Outline each blood parasite and name the species.
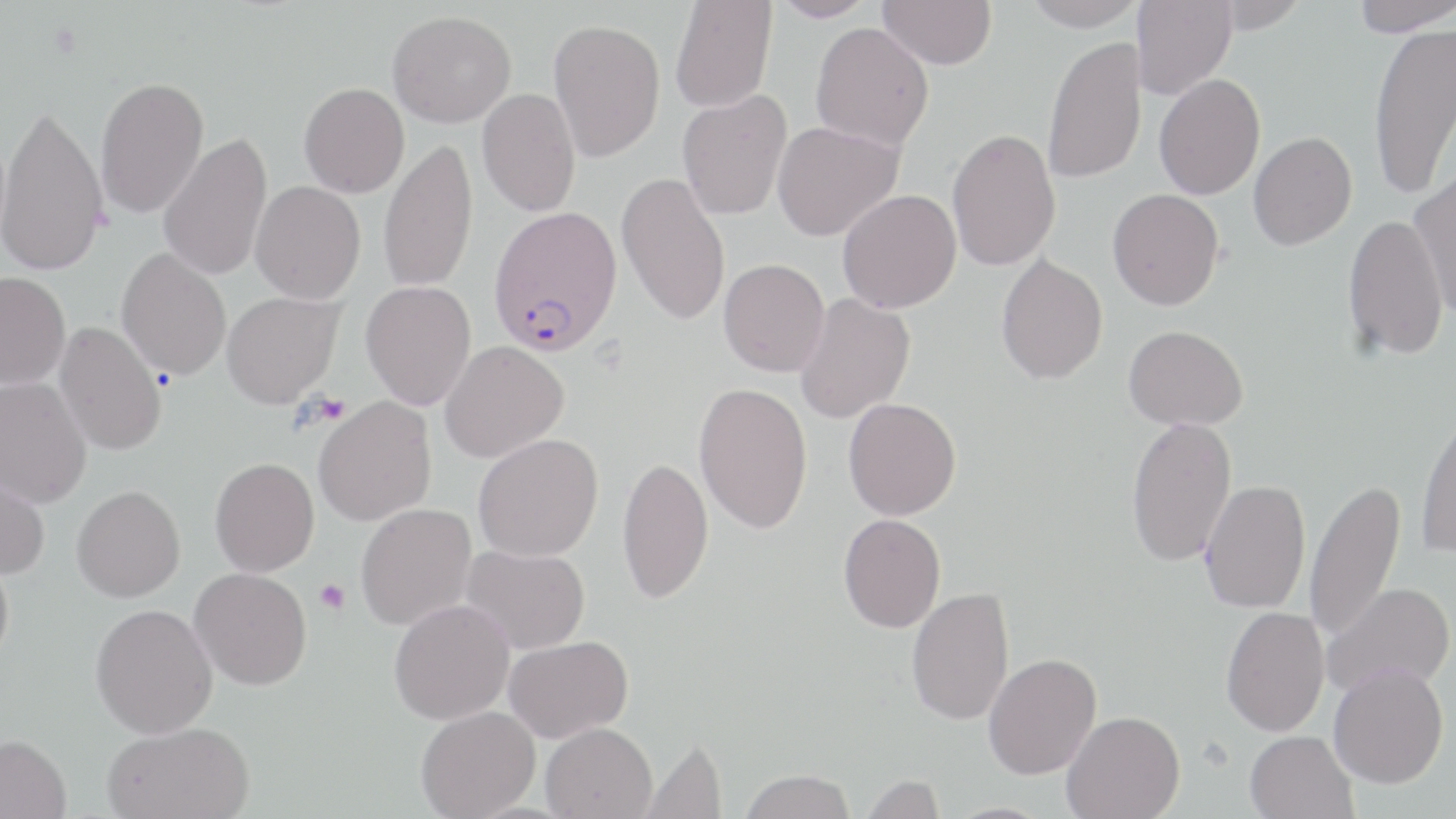

Approximate bounding boxes as [x1, y1, x2, y2] in pixels.
Plasmodium falciparum-infected red blood cells: [489, 205, 623, 356].
No Plasmodium ovale, Plasmodium malariae, Plasmodium vivax, Babesia divergens, or Trypanosoma brucei observed.

Uninfected red blood cell locations: [669, 0, 777, 113], [770, 0, 878, 22], [878, 0, 997, 70], [1021, 0, 1144, 31], [1133, 0, 1236, 100], [1207, 0, 1311, 33], [1349, 0, 1456, 37], [387, 10, 516, 128], [548, 18, 665, 161], [810, 22, 934, 152], [1368, 22, 1456, 202], [1042, 35, 1146, 184], [1153, 74, 1265, 200], [94, 76, 209, 219], [299, 82, 409, 198], [477, 89, 581, 217], [677, 90, 792, 219], [0, 102, 109, 277], [772, 121, 904, 242], [947, 128, 1061, 271], [158, 132, 273, 282], [1248, 132, 1357, 250], [378, 138, 478, 293], [1409, 169, 1456, 318], [616, 171, 731, 326], [250, 181, 366, 304], [837, 189, 962, 313], [1107, 189, 1224, 310], [1342, 214, 1449, 361], [116, 246, 232, 382], [996, 253, 1108, 385], [719, 258, 830, 377], [0, 271, 71, 389], [360, 280, 476, 409], [222, 292, 343, 408], [794, 292, 916, 424], [53, 321, 168, 456], [1124, 325, 1248, 430], [440, 341, 568, 462], [0, 377, 93, 508], [694, 382, 813, 534], [313, 396, 436, 526], [843, 398, 961, 520], [1415, 407, 1456, 559], [1125, 416, 1237, 566], [473, 433, 604, 561], [617, 456, 714, 604], [210, 457, 319, 576], [0, 466, 50, 581], [1304, 478, 1405, 645], [1199, 479, 1311, 613], [72, 485, 185, 602], [355, 503, 477, 631], [838, 513, 946, 633], [460, 544, 590, 654], [0, 549, 14, 670], [189, 567, 312, 690], [1323, 583, 1454, 698], [906, 587, 1014, 725], [388, 599, 514, 724], [90, 603, 218, 738], [1221, 606, 1330, 736], [504, 635, 633, 741], [983, 653, 1102, 779], [1329, 663, 1449, 789], [415, 706, 540, 819], [1062, 710, 1185, 819], [101, 721, 255, 819], [541, 722, 657, 819], [1245, 730, 1359, 819], [0, 734, 72, 819], [638, 735, 727, 819], [738, 769, 856, 819], [858, 773, 946, 817]. Platelet locations: [312, 394, 350, 425], [314, 579, 350, 614]. Slide-level diagnosis: Plasmodium falciparum. One field of a larger specimen. Image is 1456×819 pixels. Thin blood film. Optical microscopy. 1000x magnification. May-Grünwald-Giemsa-stained preparation.